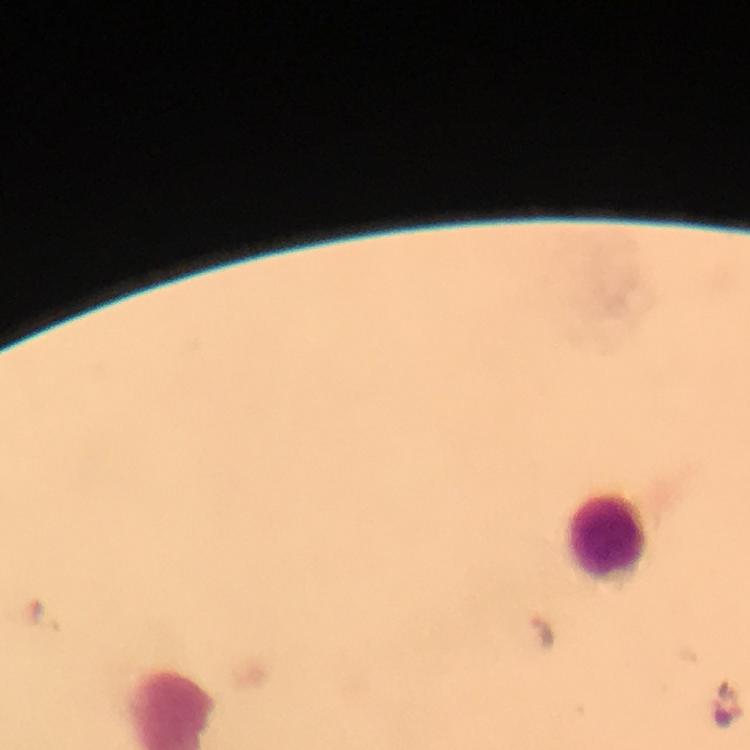

immersion oil = used
cropped from = one field of view
stain = Giemsa
preparation = thick blood smear
leukocyte locations = approximate centers as (x, y) in pixels: (606, 534)
context = from a malaria diagnostic workup
Plasmodium parasite locations = approximate centers as (x, y) in pixels: (544, 634)
image size = 750×750 pixels
capture = smartphone photograph through a microscope
magnification = 100x